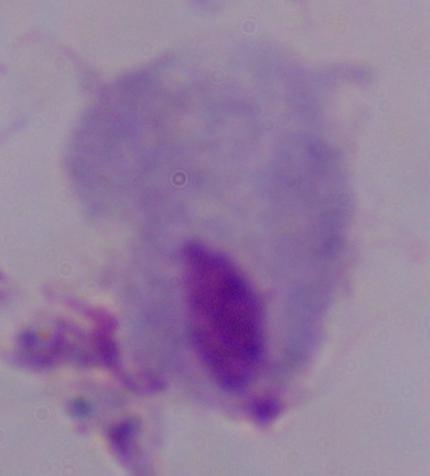

1000x magnification. Micrograph. A trichomonad is seen.